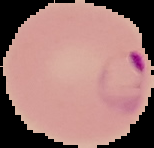
Image is 154×148 pixels. Segmented cell region on a black background. Result: Plasmodium parasites detected. From a thin blood smear.